Identify the parasite.
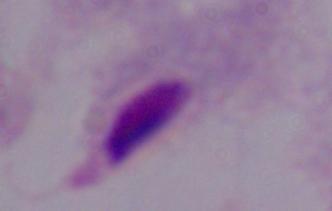
This is a trichomonad.

Micrograph. Captured at 1000x magnification.